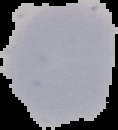

Summary:
  - Preparation: thin blood film
  - Image size: 118×130 pixels
  - Result: negative for malaria parasites
  - Image type: segmented cell region on a black background